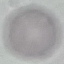

malaria status = uninfected
capture = smartphone camera at the microscope eyepiece
preparation = thin smear
image type = automatically extracted cell patch, resized to 64 × 64 pixels
stain = Giemsa